Assess this cell for malaria.
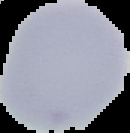

Uninfected.

image type = cell region segmented out of the field of view; surrounding area masked to black
image size = 130×133 pixels
preparation = thin blood smear